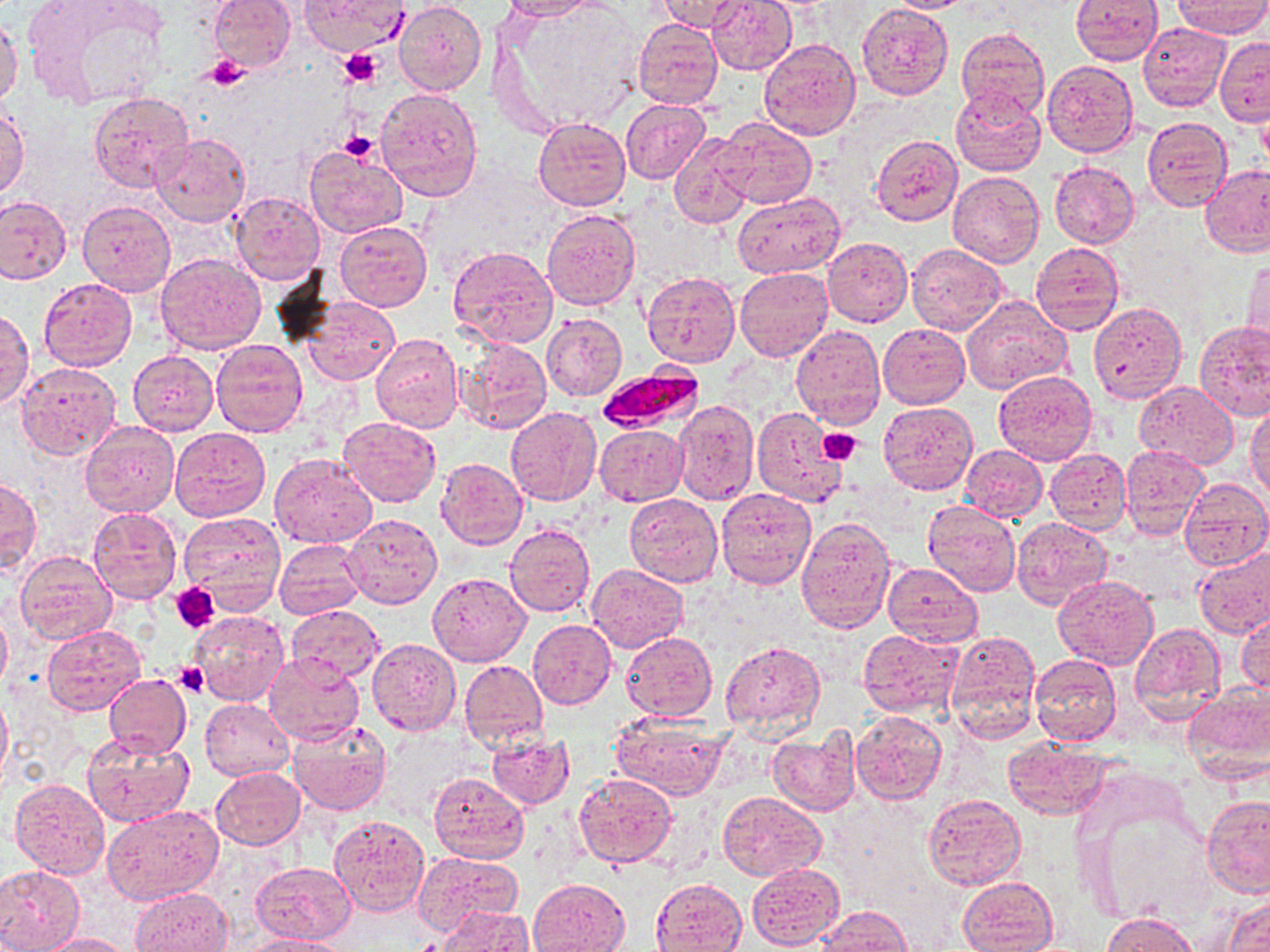

Approximate bounding boxes as named x1/y1/x2/y2 corners in pixels. Uninfected red blood cell locations: (x1=207, y1=0, x2=295, y2=72), (x1=298, y1=0, x2=409, y2=55), (x1=499, y1=0, x2=600, y2=21), (x1=655, y1=0, x2=749, y2=32), (x1=705, y1=0, x2=796, y2=74), (x1=881, y1=0, x2=982, y2=13), (x1=1070, y1=0, x2=1162, y2=64), (x1=394, y1=1, x2=486, y2=96), (x1=1173, y1=1, x2=1270, y2=37), (x1=857, y1=3, x2=954, y2=100), (x1=35, y1=4, x2=171, y2=108), (x1=0, y1=15, x2=23, y2=107), (x1=633, y1=19, x2=722, y2=109), (x1=1138, y1=23, x2=1231, y2=112), (x1=956, y1=27, x2=1051, y2=119), (x1=1216, y1=36, x2=1269, y2=126), (x1=758, y1=37, x2=862, y2=141), (x1=1041, y1=59, x2=1137, y2=157), (x1=376, y1=87, x2=483, y2=200), (x1=948, y1=88, x2=1046, y2=176), (x1=89, y1=91, x2=194, y2=192), (x1=621, y1=99, x2=709, y2=182), (x1=0, y1=103, x2=28, y2=200), (x1=1257, y1=107, x2=1270, y2=174), (x1=534, y1=116, x2=630, y2=210), (x1=1142, y1=116, x2=1232, y2=211), (x1=715, y1=118, x2=816, y2=208), (x1=670, y1=132, x2=756, y2=228), (x1=150, y1=133, x2=250, y2=226), (x1=871, y1=134, x2=963, y2=226), (x1=306, y1=145, x2=408, y2=239), (x1=1049, y1=161, x2=1139, y2=248), (x1=1200, y1=164, x2=1270, y2=257), (x1=946, y1=169, x2=1044, y2=267), (x1=733, y1=191, x2=844, y2=276), (x1=231, y1=192, x2=325, y2=284), (x1=0, y1=196, x2=72, y2=285), (x1=77, y1=200, x2=175, y2=297), (x1=542, y1=208, x2=641, y2=310), (x1=335, y1=220, x2=432, y2=311), (x1=823, y1=236, x2=913, y2=327), (x1=1030, y1=243, x2=1125, y2=335), (x1=907, y1=244, x2=1007, y2=336), (x1=445, y1=245, x2=559, y2=351), (x1=154, y1=253, x2=266, y2=356), (x1=1243, y1=258, x2=1270, y2=353), (x1=734, y1=266, x2=833, y2=361), (x1=642, y1=271, x2=740, y2=368), (x1=39, y1=278, x2=137, y2=370), (x1=961, y1=295, x2=1072, y2=395), (x1=303, y1=296, x2=399, y2=386), (x1=1089, y1=302, x2=1187, y2=403), (x1=1, y1=309, x2=33, y2=408), (x1=541, y1=312, x2=626, y2=401), (x1=1195, y1=320, x2=1270, y2=421), (x1=790, y1=324, x2=884, y2=429), (x1=878, y1=324, x2=969, y2=408), (x1=370, y1=335, x2=463, y2=434), (x1=455, y1=337, x2=552, y2=435), (x1=211, y1=338, x2=307, y2=437), (x1=128, y1=350, x2=218, y2=435), (x1=15, y1=362, x2=122, y2=460), (x1=992, y1=370, x2=1096, y2=466), (x1=1133, y1=381, x2=1238, y2=468), (x1=671, y1=399, x2=758, y2=503), (x1=878, y1=403, x2=978, y2=495), (x1=1247, y1=403, x2=1270, y2=502), (x1=505, y1=407, x2=600, y2=506), (x1=752, y1=407, x2=849, y2=507), (x1=339, y1=417, x2=442, y2=508), (x1=81, y1=419, x2=179, y2=518), (x1=595, y1=425, x2=688, y2=505), (x1=168, y1=427, x2=270, y2=521), (x1=961, y1=445, x2=1047, y2=522), (x1=1120, y1=447, x2=1210, y2=539), (x1=1045, y1=448, x2=1131, y2=533), (x1=270, y1=454, x2=377, y2=548), (x1=436, y1=458, x2=528, y2=549), (x1=0, y1=474, x2=40, y2=575), (x1=1180, y1=479, x2=1270, y2=572), (x1=716, y1=487, x2=816, y2=588), (x1=625, y1=494, x2=723, y2=588), (x1=922, y1=500, x2=1022, y2=597), (x1=88, y1=507, x2=181, y2=604), (x1=177, y1=512, x2=286, y2=612), (x1=342, y1=512, x2=442, y2=609), (x1=796, y1=516, x2=896, y2=632), (x1=1011, y1=516, x2=1111, y2=610), (x1=506, y1=525, x2=595, y2=616), (x1=275, y1=538, x2=366, y2=621), (x1=1192, y1=545, x2=1270, y2=639), (x1=16, y1=550, x2=117, y2=647), (x1=882, y1=562, x2=982, y2=646), (x1=586, y1=563, x2=688, y2=652), (x1=427, y1=572, x2=531, y2=667), (x1=1054, y1=576, x2=1159, y2=669), (x1=288, y1=604, x2=384, y2=683), (x1=0, y1=606, x2=11, y2=695), (x1=1236, y1=607, x2=1270, y2=695), (x1=191, y1=611, x2=290, y2=706), (x1=528, y1=619, x2=616, y2=709), (x1=1128, y1=622, x2=1227, y2=723), (x1=40, y1=623, x2=147, y2=715), (x1=857, y1=628, x2=963, y2=716), (x1=945, y1=629, x2=1043, y2=742), (x1=621, y1=632, x2=717, y2=722), (x1=368, y1=638, x2=461, y2=735), (x1=721, y1=638, x2=825, y2=737), (x1=263, y1=655, x2=364, y2=747), (x1=1029, y1=656, x2=1122, y2=747), (x1=458, y1=659, x2=548, y2=751), (x1=104, y1=672, x2=191, y2=759), (x1=1181, y1=683, x2=1270, y2=784), (x1=0, y1=692, x2=11, y2=788), (x1=201, y1=700, x2=294, y2=780), (x1=852, y1=710, x2=947, y2=803), (x1=610, y1=712, x2=730, y2=799), (x1=286, y1=718, x2=393, y2=817), (x1=767, y1=730, x2=861, y2=816), (x1=82, y1=732, x2=195, y2=828), (x1=486, y1=732, x2=575, y2=810), (x1=1004, y1=737, x2=1113, y2=819), (x1=211, y1=766, x2=305, y2=849), (x1=429, y1=772, x2=528, y2=864), (x1=574, y1=772, x2=678, y2=868), (x1=9, y1=779, x2=110, y2=880), (x1=717, y1=791, x2=827, y2=880), (x1=922, y1=793, x2=1025, y2=890), (x1=1201, y1=795, x2=1270, y2=898), (x1=102, y1=805, x2=222, y2=905), (x1=1090, y1=809, x2=1212, y2=926), (x1=328, y1=814, x2=429, y2=918), (x1=413, y1=849, x2=523, y2=935), (x1=251, y1=863, x2=355, y2=944), (x1=746, y1=863, x2=845, y2=950), (x1=0, y1=866, x2=85, y2=951), (x1=958, y1=876, x2=1059, y2=951), (x1=650, y1=877, x2=747, y2=952), (x1=528, y1=879, x2=631, y2=952), (x1=131, y1=888, x2=232, y2=951), (x1=1222, y1=892, x2=1270, y2=952), (x1=815, y1=905, x2=912, y2=951), (x1=439, y1=906, x2=534, y2=952), (x1=1101, y1=913, x2=1202, y2=952), (x1=32, y1=934, x2=134, y2=952), (x1=244, y1=935, x2=349, y2=952). Platelet locations: (x1=338, y1=48, x2=383, y2=88), (x1=204, y1=55, x2=251, y2=89), (x1=341, y1=131, x2=381, y2=165), (x1=817, y1=427, x2=864, y2=467), (x1=171, y1=583, x2=220, y2=632), (x1=174, y1=661, x2=209, y2=697). Plasmodium falciparum-infected red blood cell locations: (x1=593, y1=369, x2=702, y2=433). Slide-level diagnosis: Plasmodium falciparum. Thin blood film. May-Grünwald-Giemsa-stained preparation. Image is 1270×952 pixels. Single field of view. Optical microscopy. Captured at 1000x magnification.